Report the malaria status of this cell.
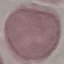
It is uninfected.

stain = Giemsa
image type = automatically extracted cell patch, resized to 64 × 64 pixels
capture = smartphone through the microscope eyepiece
preparation = thin blood smear